Point out each leukocyte.
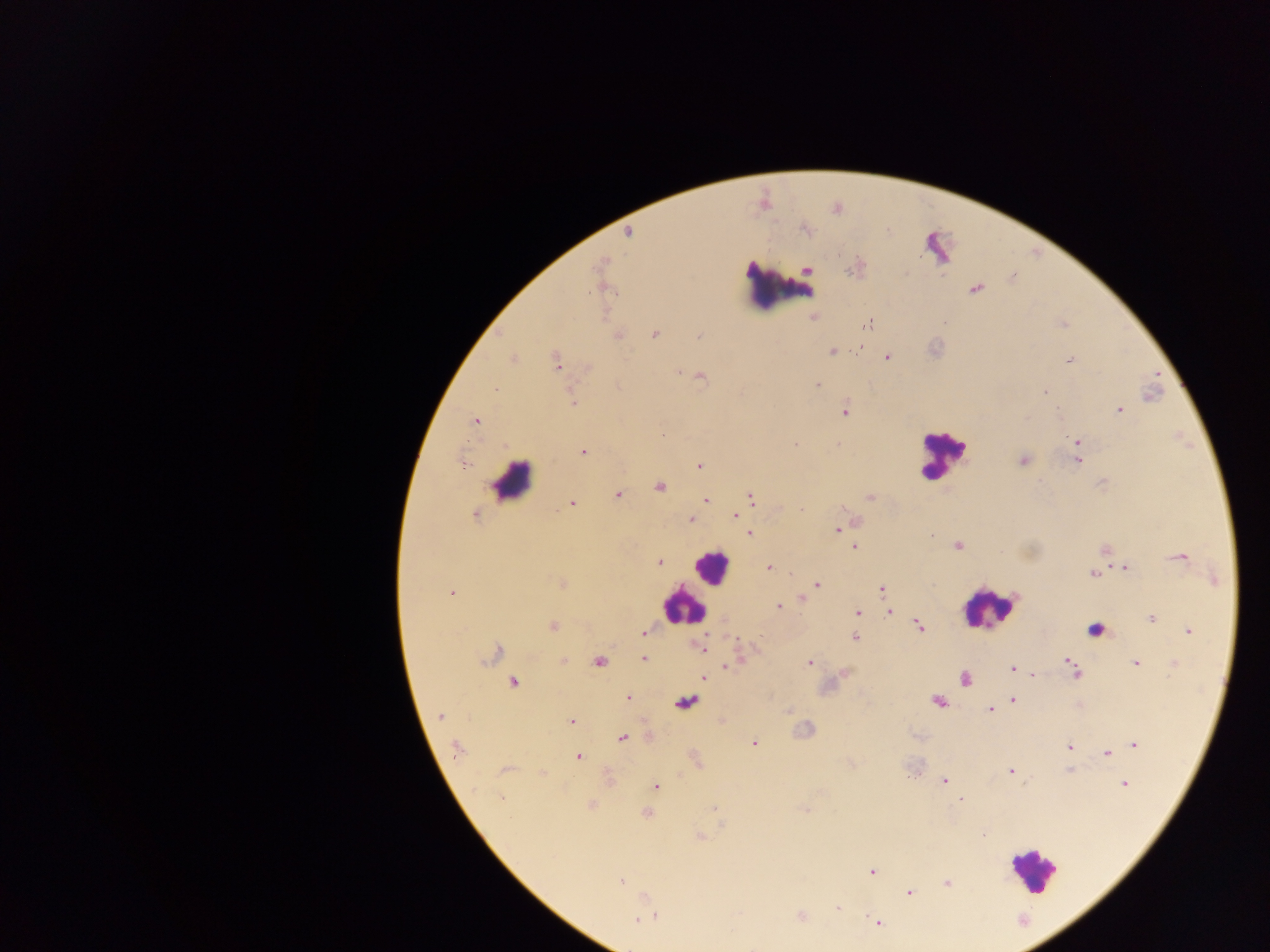
Approximate centers as (x, y) in pixels.
Leukocytes: (780, 286), (942, 455), (512, 481), (711, 566), (682, 606), (987, 607), (1094, 631), (1031, 870).

Summary:
  - Plasmodium parasite locations: (805, 229), (628, 233), (600, 265), (975, 288), (813, 318), (868, 323), (654, 334), (618, 335), (699, 335), (860, 347), (832, 351), (887, 357), (513, 359), (1069, 360), (556, 362), (588, 368), (678, 372), (701, 377), (818, 385), (495, 389), (1045, 392), (572, 403), (1120, 410), (845, 411), (476, 421), (662, 435), (1078, 441), (796, 444), (583, 452), (1023, 461), (1077, 461), (463, 464), (700, 466), (660, 487), (618, 494), (751, 498), (870, 498), (706, 500), (572, 503), (802, 508), (474, 515), (735, 517), (691, 520), (837, 529), (748, 533), (957, 545), (855, 547), (1180, 557), (660, 563), (770, 568), (1125, 568), (1092, 574), (560, 584), (816, 584), (882, 589), (452, 592), (803, 598), (779, 606), (889, 611), (858, 612), (1150, 619), (553, 626), (918, 626), (1189, 631), (644, 633), (854, 638), (700, 647), (496, 653), (643, 658), (1068, 660), (564, 661), (599, 662), (809, 663), (1136, 664), (727, 666), (1072, 666), (1012, 669), (1076, 673), (1033, 674), (704, 677), (965, 678), (513, 682), (628, 697), (1013, 700), (937, 702), (687, 703), (990, 710), (440, 715), (571, 722), (622, 737), (754, 744), (1135, 745), (1069, 746), (457, 749), (1107, 753), (578, 757), (504, 769), (1011, 771), (944, 781), (1124, 784), (656, 786), (501, 798), (961, 799), (712, 809), (805, 810), (647, 813), (700, 837), (872, 872), (620, 881), (947, 882), (909, 893), (838, 908), (801, 916), (651, 917), (640, 920), (877, 922)
  - Capture: mobile-phone photograph through a microscope
  - Field of view: single
  - Country: Ghana
  - Image size: 1270×952 pixels
  - Preparation: thick blood smear